Assess for malaria.
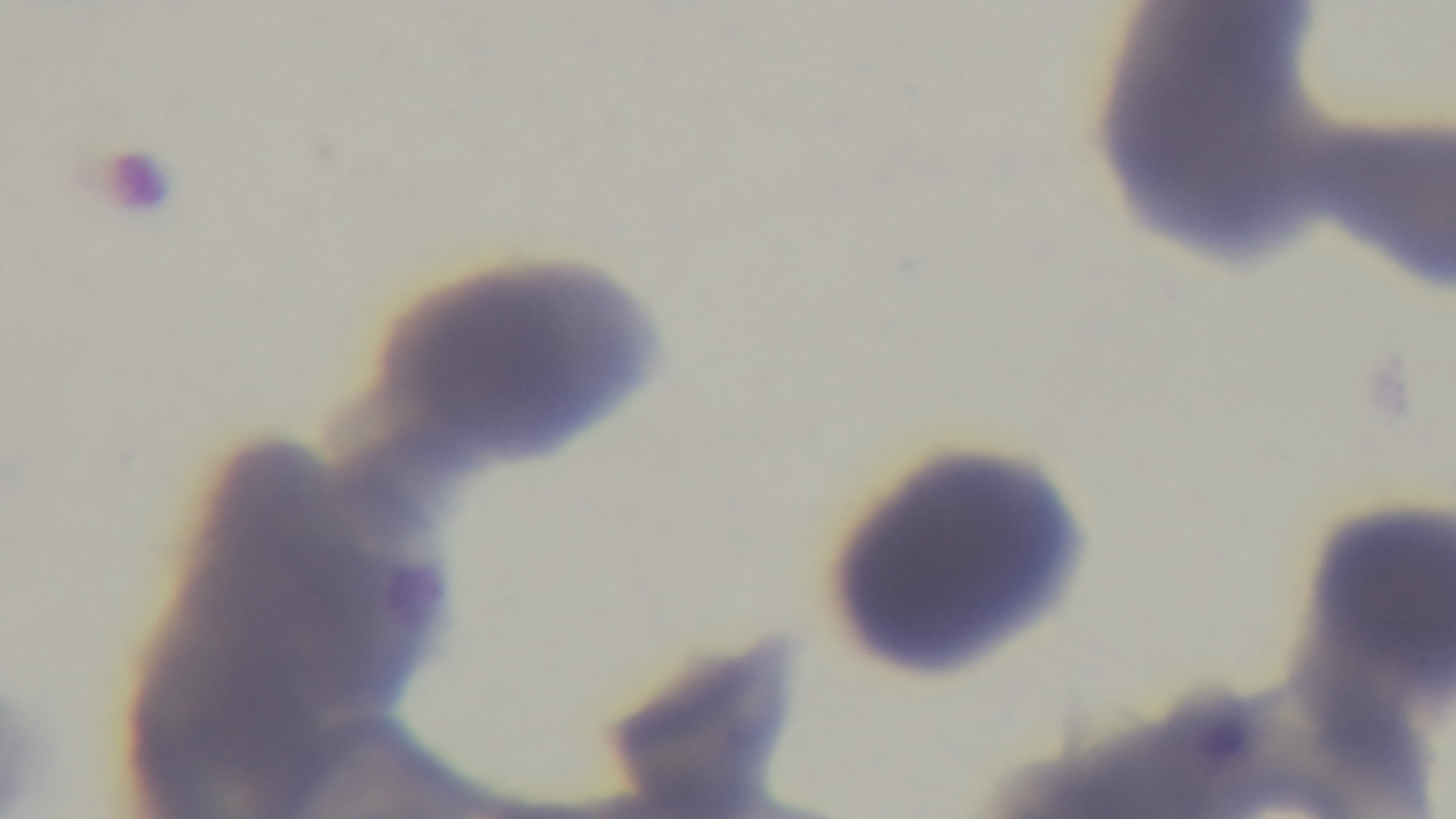

Negative.

Preparation: thin smear. Photomicrograph. Giemsa-stained. Single field of view. Mounted 4K digital camera. 100x oil-immersion objective.